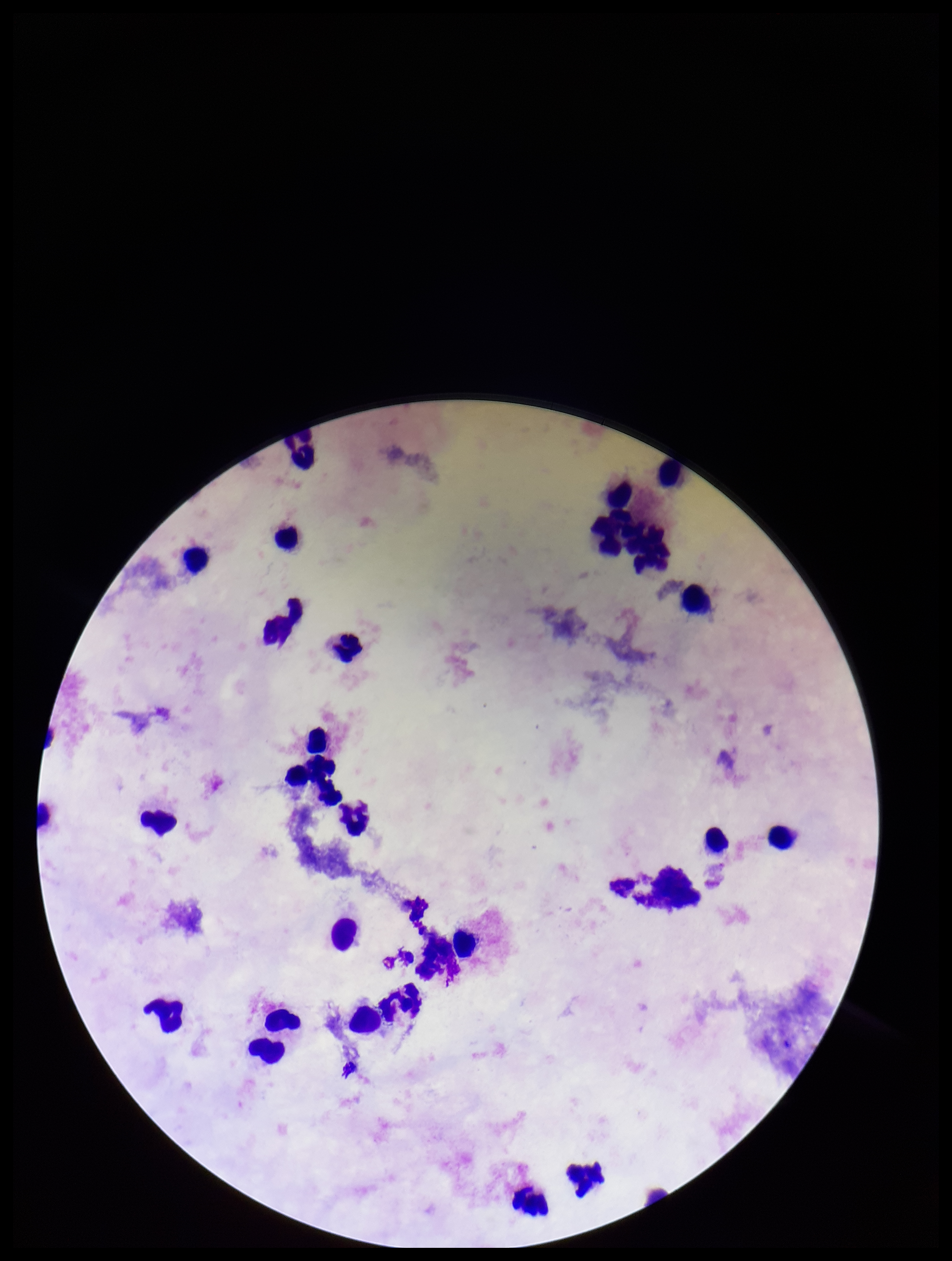

Smartphone photograph taken through the eyepiece of a microscope. Preparation: thick smear. Stained with Giemsa. Image is 952×1261 pixels. Leukocyte count: 26. Parasite count: 0. One field from this slide. Patient malaria status: negative. Plasmodium parasites: none seen.